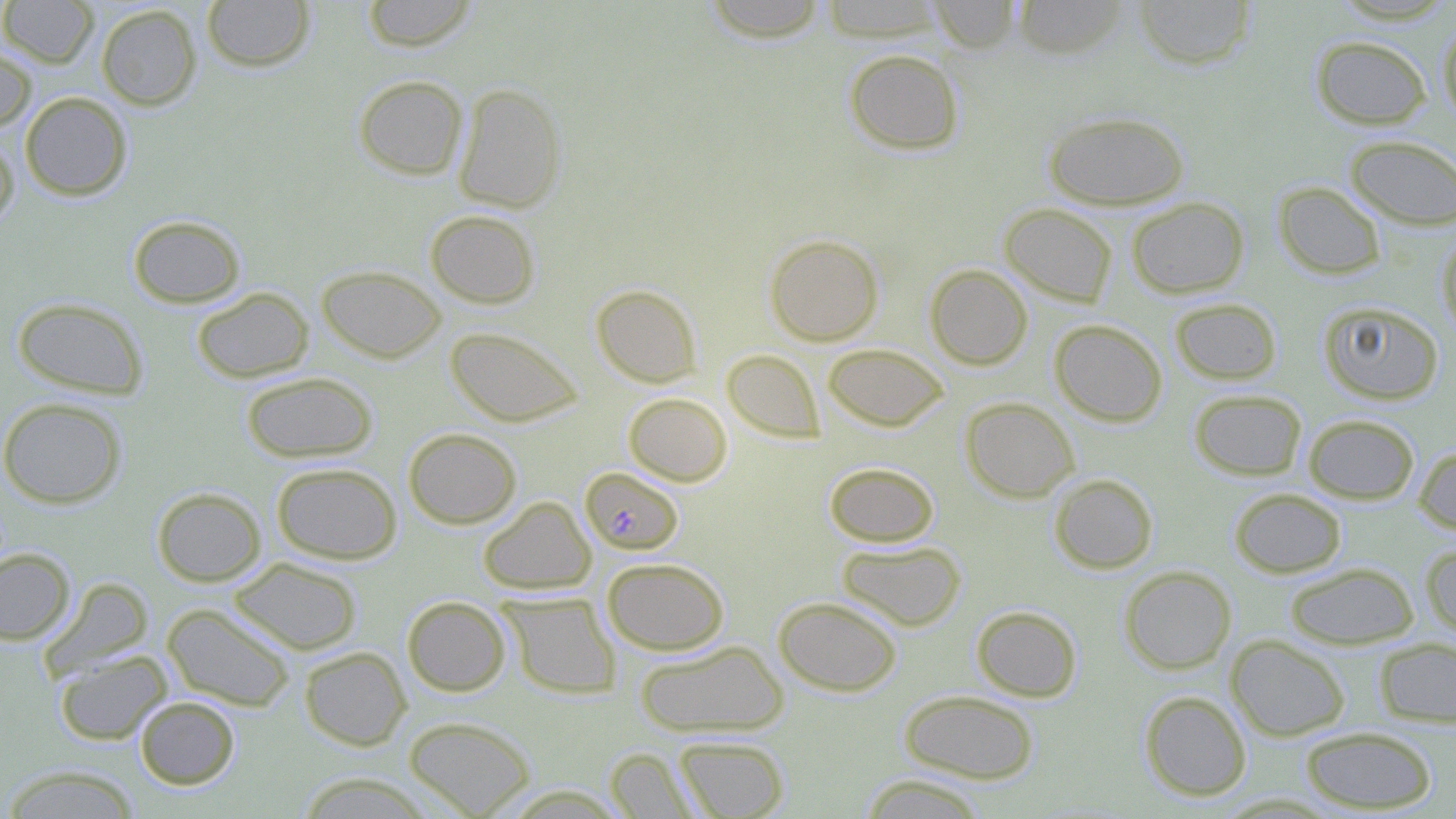

Approximate bounding boxes as (x1,y1)-(x2,y2) corner pairs in pixels. Uninfected red blood cell locations: (0,0)-(98,67), (201,0)-(315,72), (361,0)-(478,52), (700,0)-(830,42), (819,0)-(948,42), (928,0)-(1023,53), (1132,0)-(1257,70), (1011,1)-(1130,59), (96,4)-(201,110), (1437,21)-(1456,127), (1310,35)-(1432,129), (0,42)-(37,131), (843,48)-(965,155), (353,74)-(468,180), (452,82)-(567,213), (20,92)-(132,201), (1042,110)-(1190,210), (0,131)-(19,233), (1344,135)-(1456,230), (1273,181)-(1386,279), (1127,196)-(1249,298), (1000,203)-(1118,307), (425,209)-(540,308), (127,214)-(246,308), (1436,232)-(1456,341), (764,234)-(884,346), (925,263)-(1032,369), (316,265)-(446,363), (590,284)-(702,387), (191,287)-(313,383), (12,297)-(149,400), (1170,297)-(1282,385), (1318,301)-(1444,405), (1049,319)-(1167,426), (445,326)-(583,427), (822,343)-(949,432), (722,349)-(824,443), (240,371)-(378,463), (1189,389)-(1307,480), (623,392)-(732,486), (0,397)-(127,509), (960,397)-(1080,502), (1303,413)-(1419,504), (403,427)-(522,528), (1414,444)-(1456,536), (824,461)-(940,547), (271,462)-(402,564), (1048,473)-(1158,573), (152,486)-(266,586), (1229,488)-(1346,578), (478,496)-(596,595), (836,539)-(966,631), (1421,542)-(1456,639), (0,548)-(75,645), (229,557)-(362,655), (602,557)-(730,655), (1285,562)-(1419,650), (1119,566)-(1236,674), (40,577)-(154,679), (500,593)-(621,699), (402,595)-(511,696), (774,595)-(903,696), (162,603)-(296,711), (971,605)-(1082,702), (1227,635)-(1350,741), (1374,637)-(1456,727), (634,640)-(788,737), (299,646)-(411,750), (54,650)-(173,745), (898,689)-(1039,784), (1139,690)-(1252,801), (134,696)-(239,789), (403,715)-(536,817), (1301,726)-(1438,813), (674,736)-(789,818), (605,747)-(700,818), (1,764)-(143,818), (294,772)-(434,818), (857,773)-(991,818). Plasmodium falciparum-infected red blood cell locations: (580,466)-(684,555). Slide-level diagnosis: Plasmodium falciparum. Single field of view. Optical microscopy. Thin blood smear. May-Grünwald-Giemsa stain. Captured at 1000x magnification. Image is 1456×819 pixels.